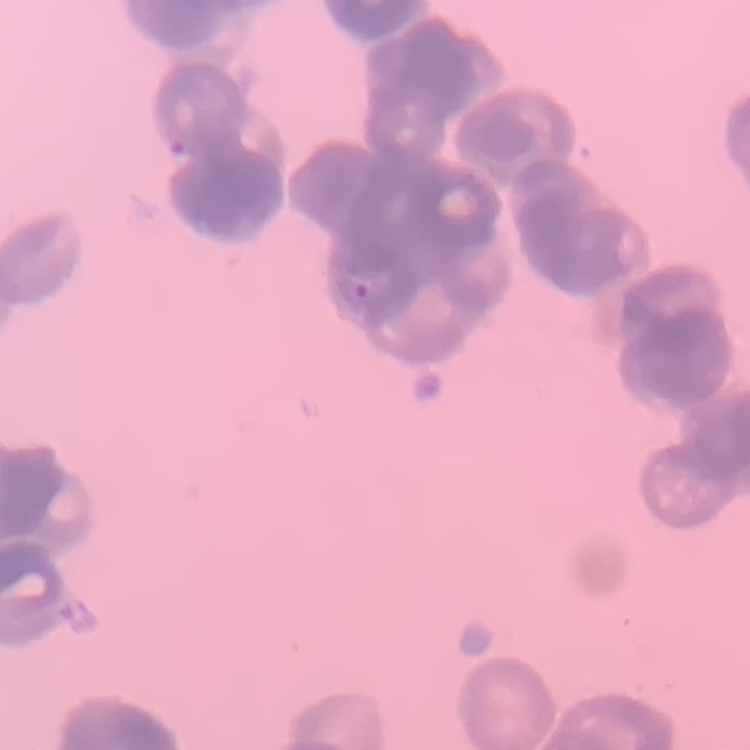 The red blood cells show rouleaux formation. Stained with either Field's or Giemsa. Thin peripheral smear. One tile cut from a larger photomicrograph.